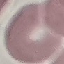

result = no malaria parasites detected
capture = smartphone through the microscope eyepiece
stain = Giemsa
image type = cell patch, automatically extracted from a larger field of view and resized to 64 × 64 pixels
preparation = thin blood film